Report the malaria status of this cell.
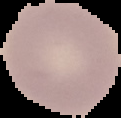

Uninfected.

image type = segmented cell region on a black background
image size = 121×118 pixels
preparation = thin blood smear